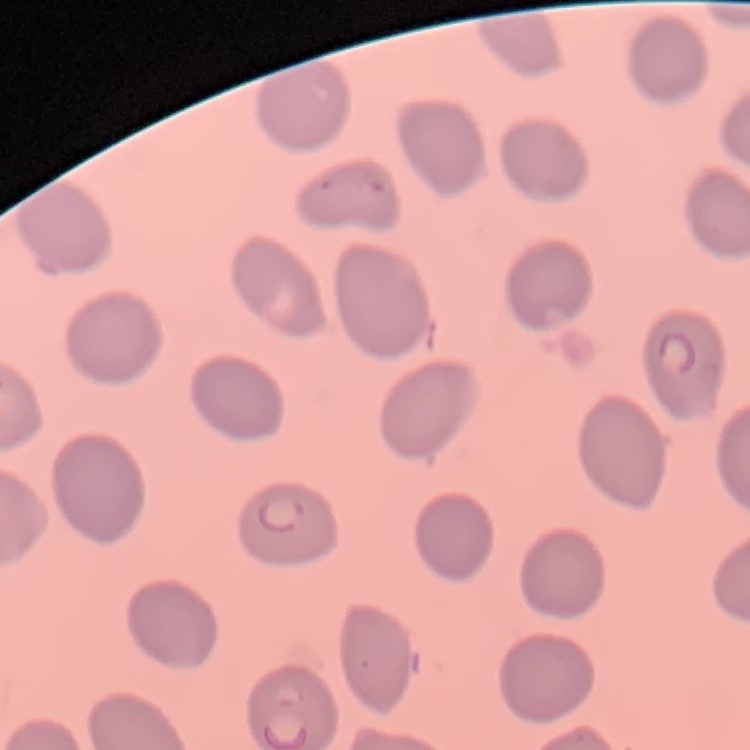

Summary:
  - Red blood cell morphology: no rouleaux formation
  - Preparation: thin blood smear
  - Image type: one tile cut from a larger photomicrograph
  - Stain: Field's or Giemsa